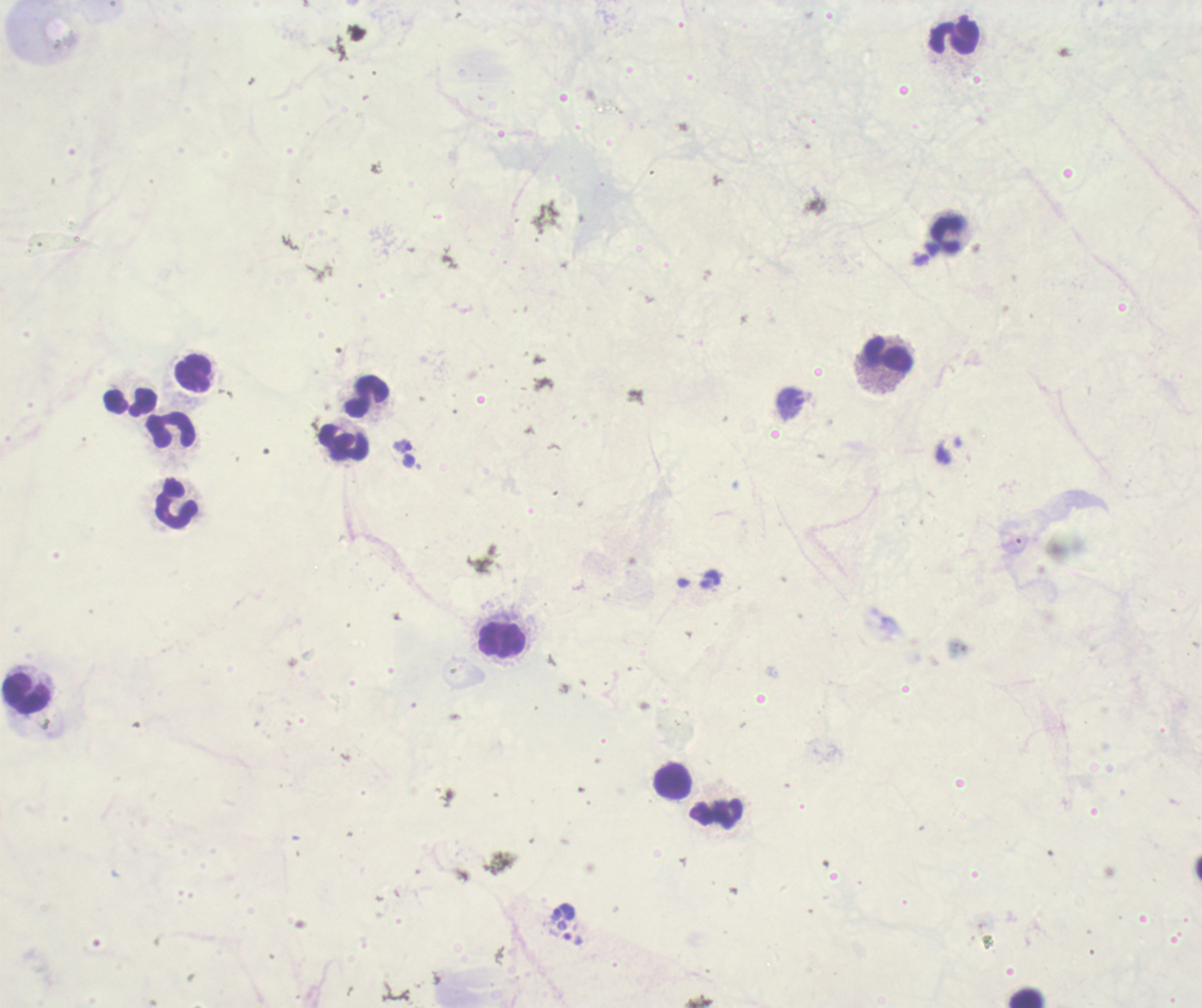
coordinate format = approximate object centers, in pixels from the top-left corner
trophozoite locations = (x=790, y=403), (x=403, y=445)
leukocyte locations = (x=954, y=37), (x=946, y=234), (x=888, y=355), (x=193, y=373), (x=366, y=397), (x=131, y=401), (x=171, y=429), (x=344, y=443), (x=176, y=503), (x=501, y=640), (x=26, y=695), (x=673, y=782), (x=716, y=813), (x=1028, y=998)
coloration quality = bad
result = Plasmodium parasites detected
field of view = one from this slide
stain = Romanowsky
background quality = poor
context = previously used in a real diagnosis
magnification = 100x
image size = 1202×1008 pixels
preparation = thick blood smear